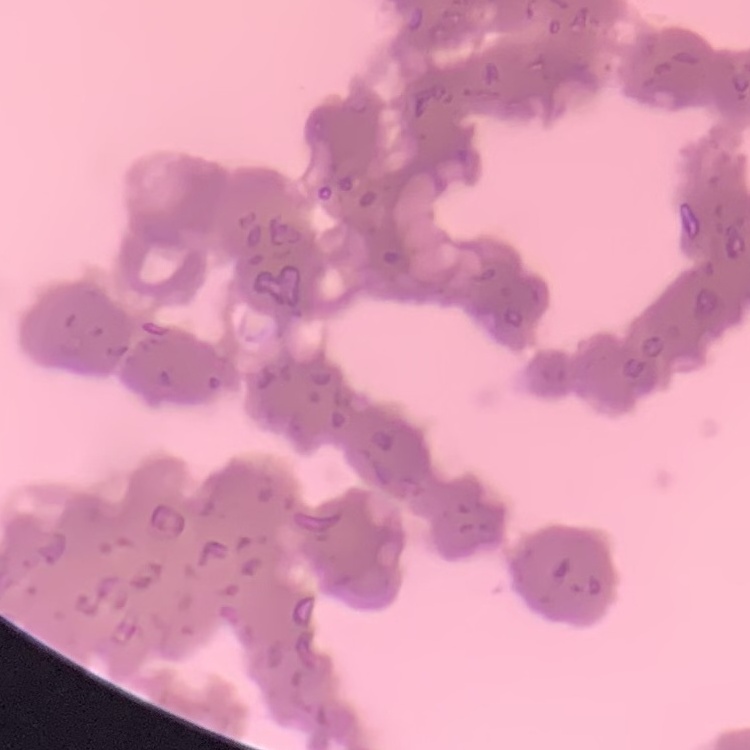
Summary:
  - Erythrocyte morphology: rouleaux formation
  - Stain: Field's or Giemsa
  - Image type: square crop of a larger photomicrograph
  - Preparation: thin peripheral smear